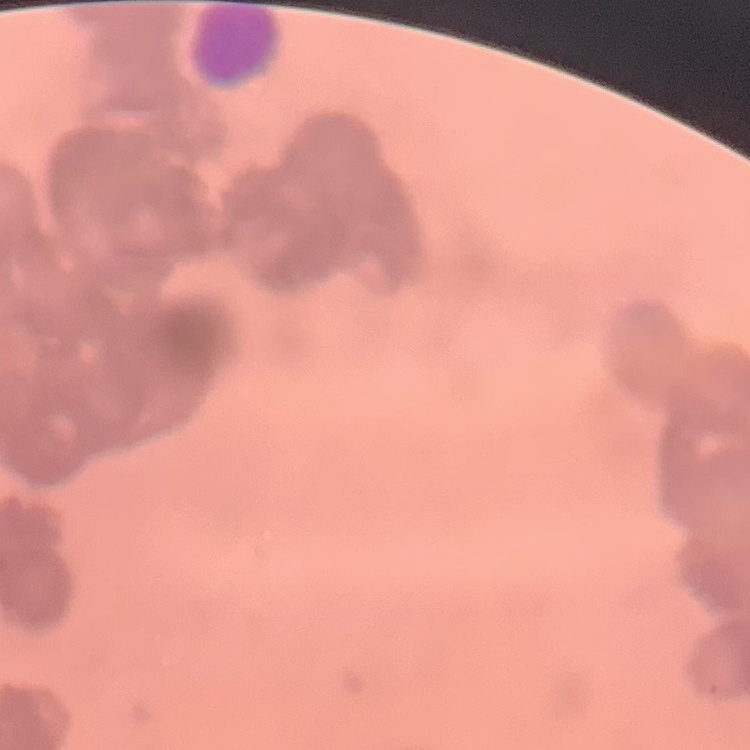

erythrocyte_morphology: rouleaux formation
preparation: thin peripheral smear
stain: Field's or Giemsa
image_type: one tile cut from a larger photomicrograph